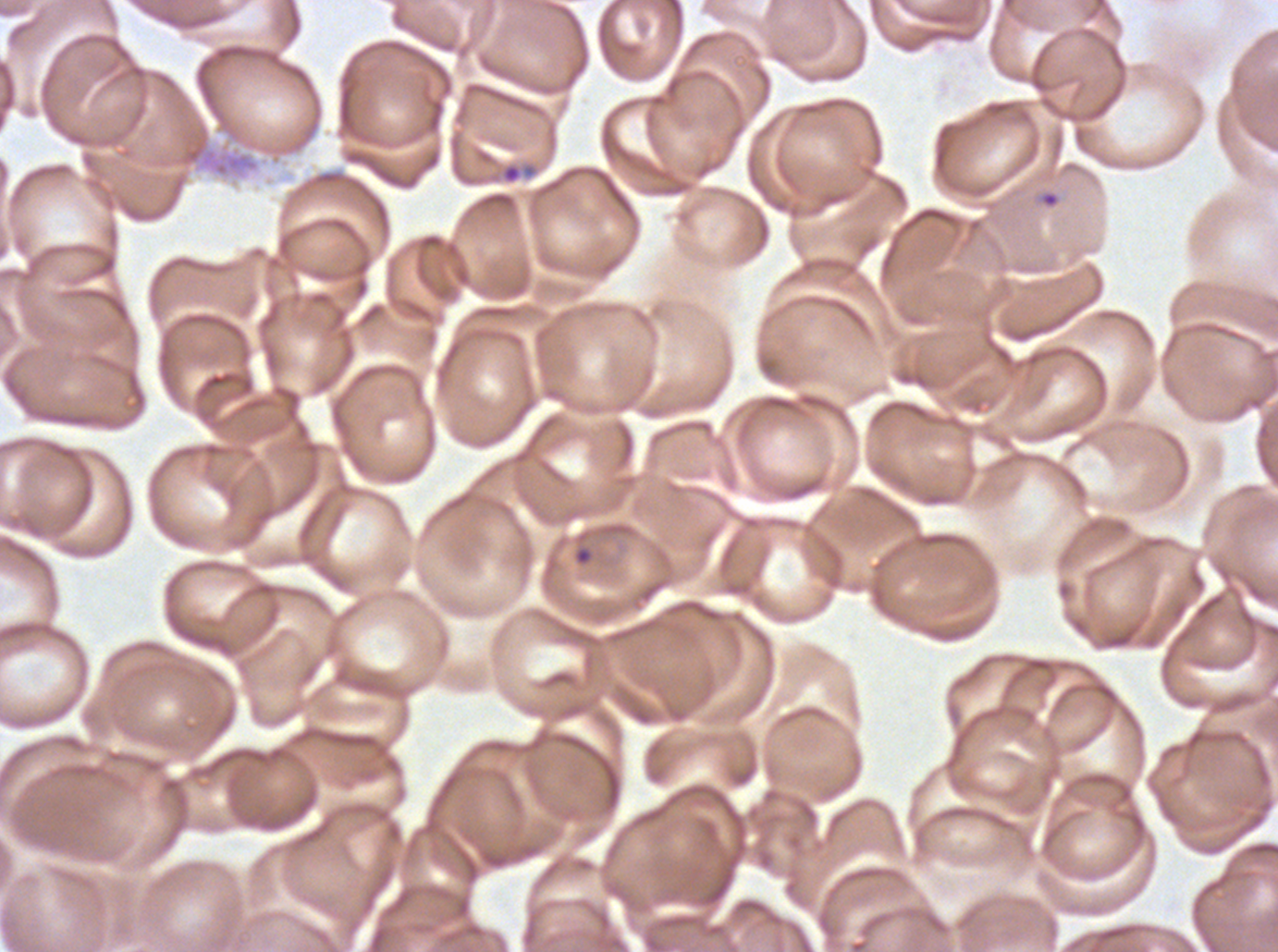

field_of_view: one sub-image of a larger composite
specimen: Plasmodium falciparum cultured ex vivo for 24 to 48 hours, from a patient in The Gambia
stain: Giemsa
image_size: 1278×952 pixels
ring_locations: 'approximate bounding boxes as {x1, y1, x2, y2} in pixels: {501, 164, 522, 184}, {1039, 190, 1060, 209}'
preparation: thin blood smear